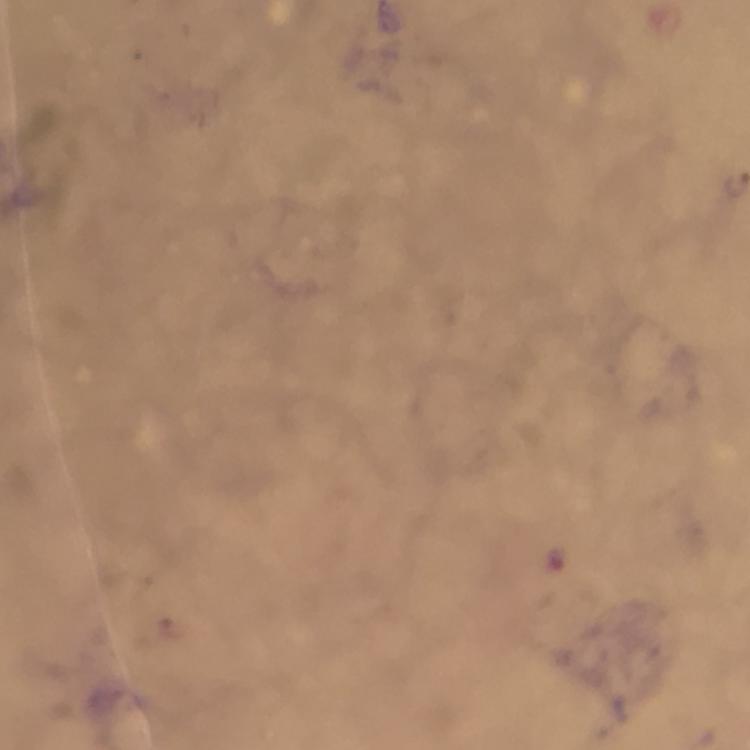 Approximate centers as [x, y] in pixels. Plasmodium parasite locations: [175, 627]. 100x magnification. Thick smear. Immersion oil was used. Image is 750×750 pixels. Giemsa-stained preparation. Cropped region of a single field of view. Photographed through the microscope with a smartphone camera. From a diagnostic examination for malaria.